State which parasite is depicted.
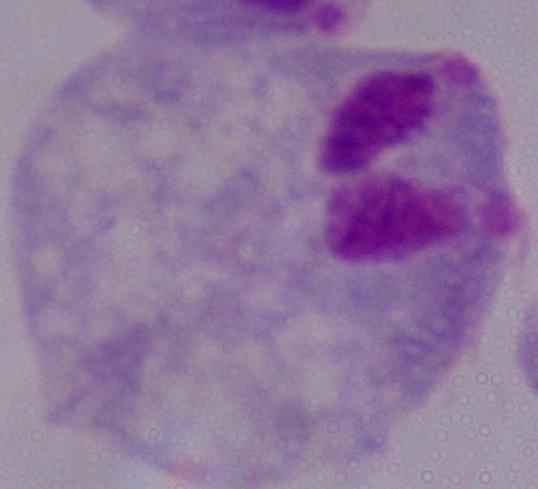
This is a trichomonad.

Micrograph. 1000x magnification.